Locate and identify every blood parasite.
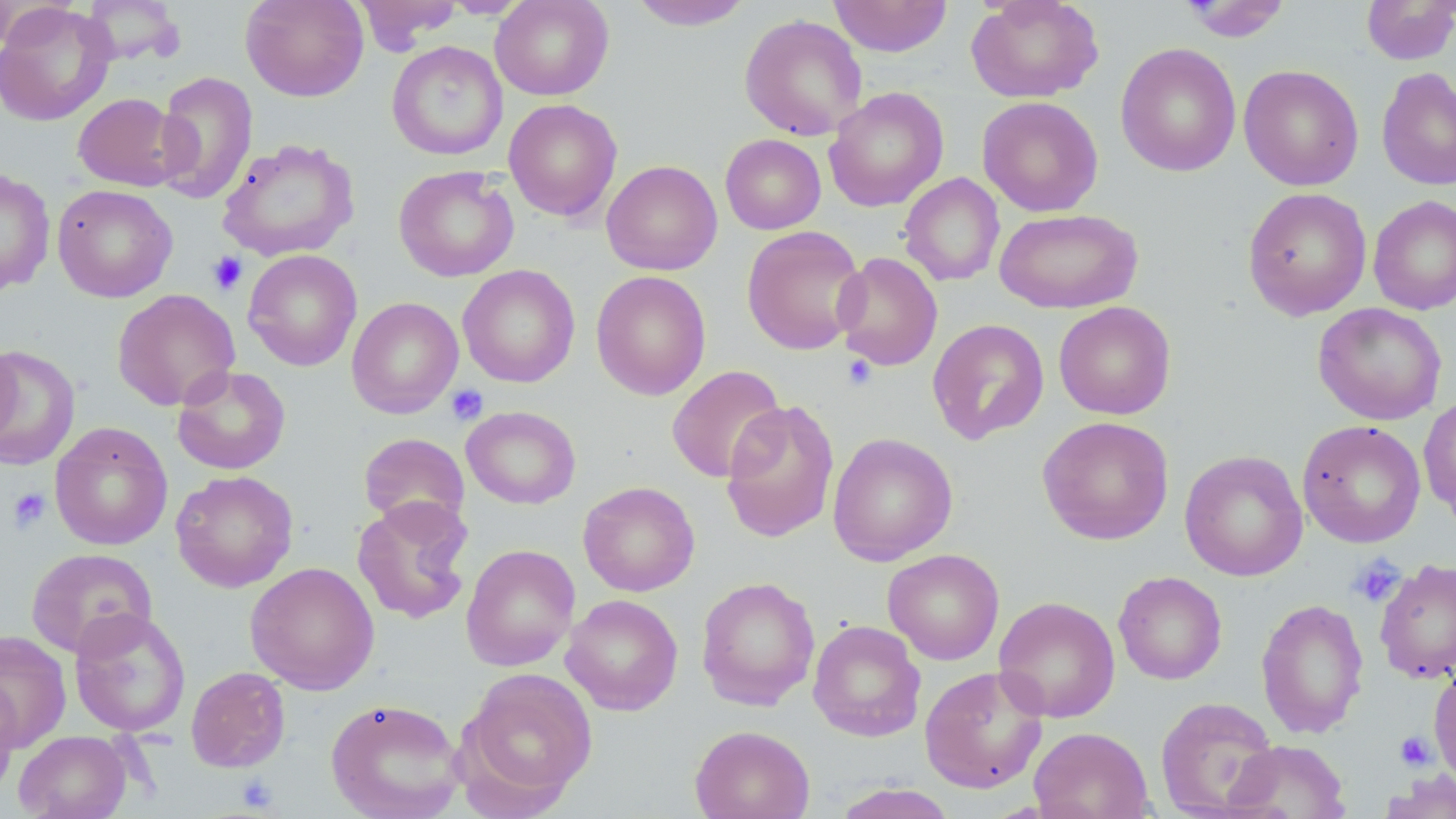

No blood parasites seen.

slide-level diagnosis = no evidence of blood parasites
preparation = thin blood film
platelet locations = approximate bounding boxes as (x1,y1)-(x2,y2) corner pairs in pixels: (207,251)-(248,295), (841,354)-(878,390), (447,384)-(489,426), (7,487)-(51,534), (1348,554)-(1407,608), (1395,730)-(1436,770), (235,773)-(280,812)
modality = optical microscopy
field of view = one of a larger specimen
stain = May-Grünwald-Giemsa
image size = 1456×819 pixels
uninfected red blood cell locations = approximate bounding boxes as (x1,y1)-(x2,y2) corner pairs in pixels: (80,0)-(186,66), (241,0)-(368,102), (352,0)-(461,52), (441,0)-(532,18), (490,0)-(614,101), (829,0)-(952,57), (966,0)-(1104,102), (1179,0)-(1292,42), (1360,0)-(1456,65), (628,1)-(754,31), (0,3)-(116,126), (739,14)-(867,141), (387,41)-(508,161), (1115,43)-(1241,177), (1238,65)-(1364,190), (1376,67)-(1456,191), (153,70)-(258,205), (824,88)-(949,212), (72,93)-(184,192), (977,96)-(1103,216), (504,99)-(622,222), (720,133)-(826,234), (217,138)-(359,262), (601,159)-(722,276), (393,165)-(519,282), (0,167)-(55,296), (899,173)-(1005,287), (52,184)-(178,303), (1242,187)-(1372,320), (1368,194)-(1456,315), (996,208)-(1142,314), (741,225)-(867,355), (243,249)-(362,371), (833,252)-(943,370), (457,264)-(580,388), (590,270)-(711,400), (112,289)-(240,411), (346,297)-(463,419), (1054,301)-(1176,420), (1313,303)-(1447,424), (927,318)-(1049,445), (0,339)-(20,452), (0,345)-(80,471), (172,365)-(291,475), (667,365)-(786,483), (1418,394)-(1456,519), (720,398)-(840,544), (462,406)-(581,509), (1037,416)-(1174,545), (1297,420)-(1426,548), (50,422)-(173,550), (358,432)-(470,533), (828,432)-(958,566), (1180,450)-(1308,581), (170,470)-(298,592), (578,480)-(700,597), (352,496)-(474,625), (461,544)-(580,671), (25,548)-(157,658), (882,548)-(1005,665), (1374,559)-(1456,685), (245,561)-(380,694), (1113,571)-(1227,685), (696,575)-(820,711), (561,594)-(683,715), (993,596)-(1120,723), (1256,597)-(1369,739), (69,608)-(191,737), (808,620)-(926,742), (0,630)-(72,752), (1429,665)-(1456,791), (185,666)-(291,772), (919,666)-(1048,794), (459,668)-(598,808), (0,673)-(21,799), (1155,696)-(1280,818), (325,697)-(465,819), (689,725)-(815,819), (1029,726)-(1154,819), (14,730)-(131,819), (1226,739)-(1351,819), (1379,770)-(1456,819), (830,783)-(958,819)
magnification = 1000x